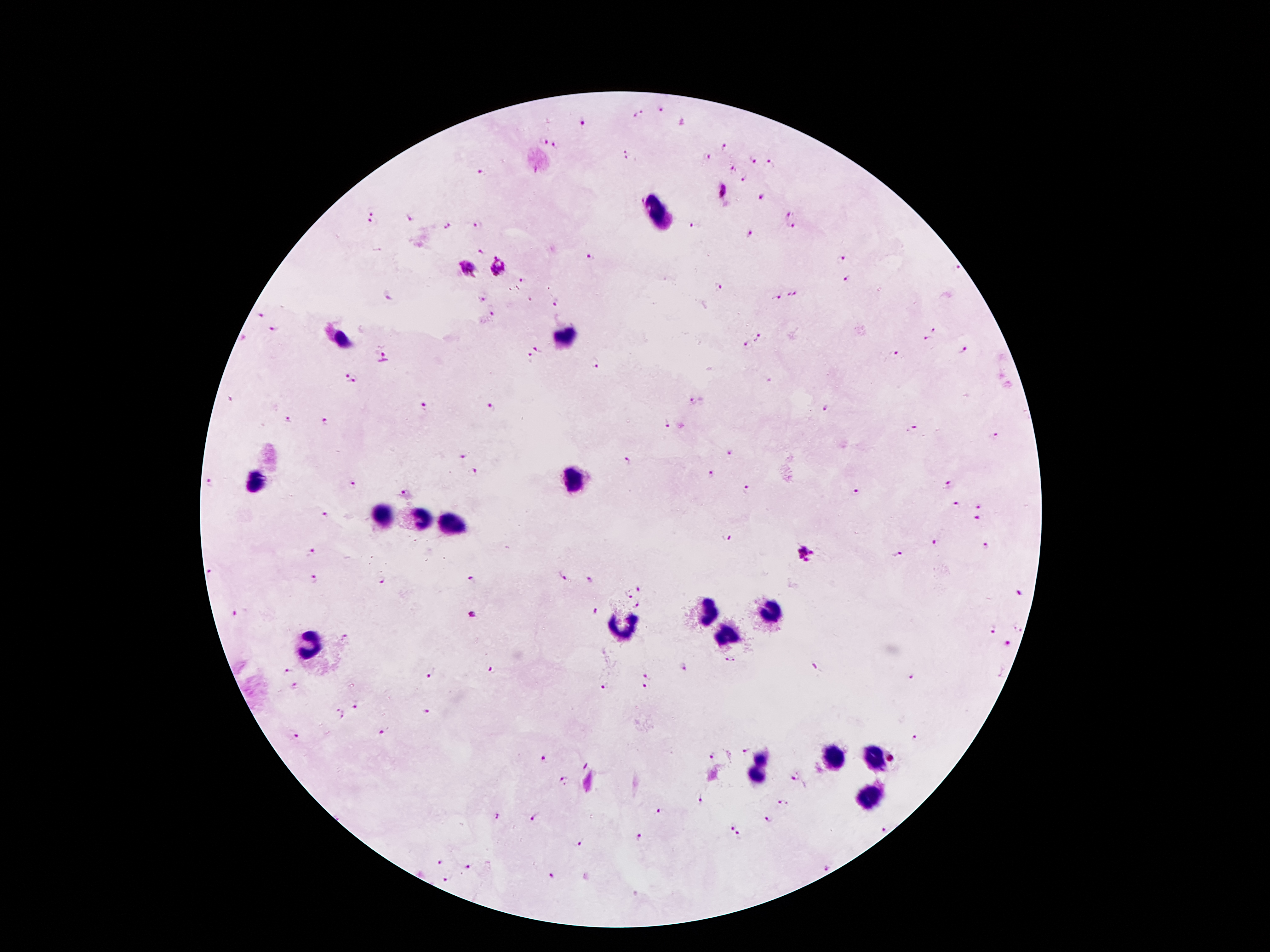
Patient malaria status: positive for Plasmodium falciparum. 100x magnification. Smartphone photograph taken through the microscope eyepiece. Giemsa stain. One field from this slide. Thick blood smear. Image is 1270×952 pixels.